Point out Plasmodium parasites and leukocytes.
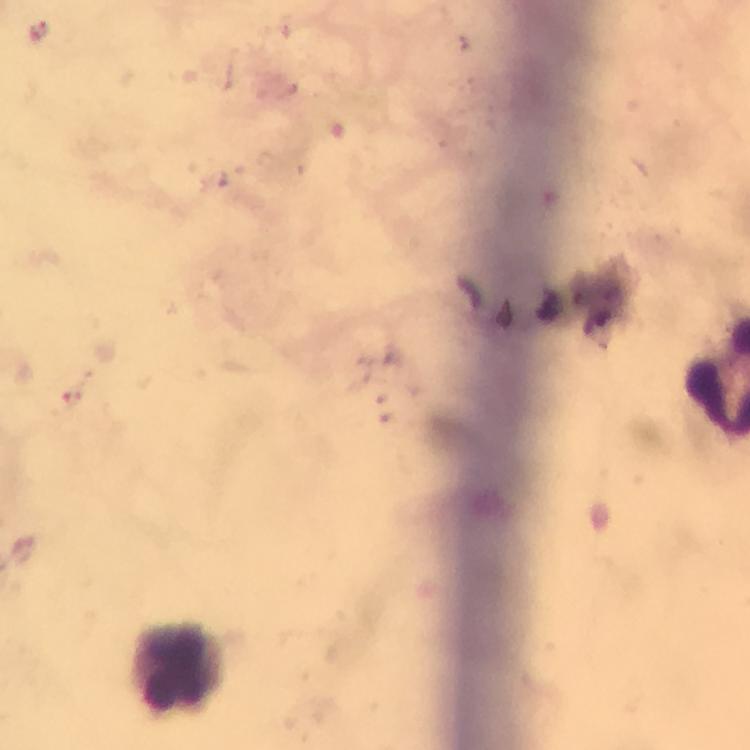
Approximate centers as [x, y] in pixels.
Plasmodium parasites: [39, 33].
Leukocytes: [178, 664].

{
  "stain": "Giemsa",
  "cropped_from": "one field of view",
  "preparation": "thick blood smear",
  "capture": "smartphone camera through the microscope",
  "immersion_oil": "used",
  "image_size": "750×750 pixels",
  "context": "from a diagnostic examination for malaria",
  "magnification": "100x"
}